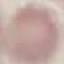 Malaria status: uninfected. Cell patch, automatically extracted from a larger field of view and resized to 64 × 64 pixels. Giemsa-stained preparation. Photographed with a smartphone camera at the microscope eyepiece. Thin blood film.